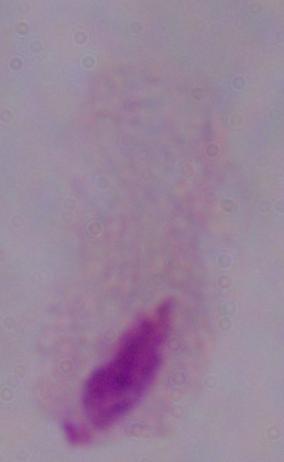

identification = trichomonad
modality = micrograph
magnification = 1000x